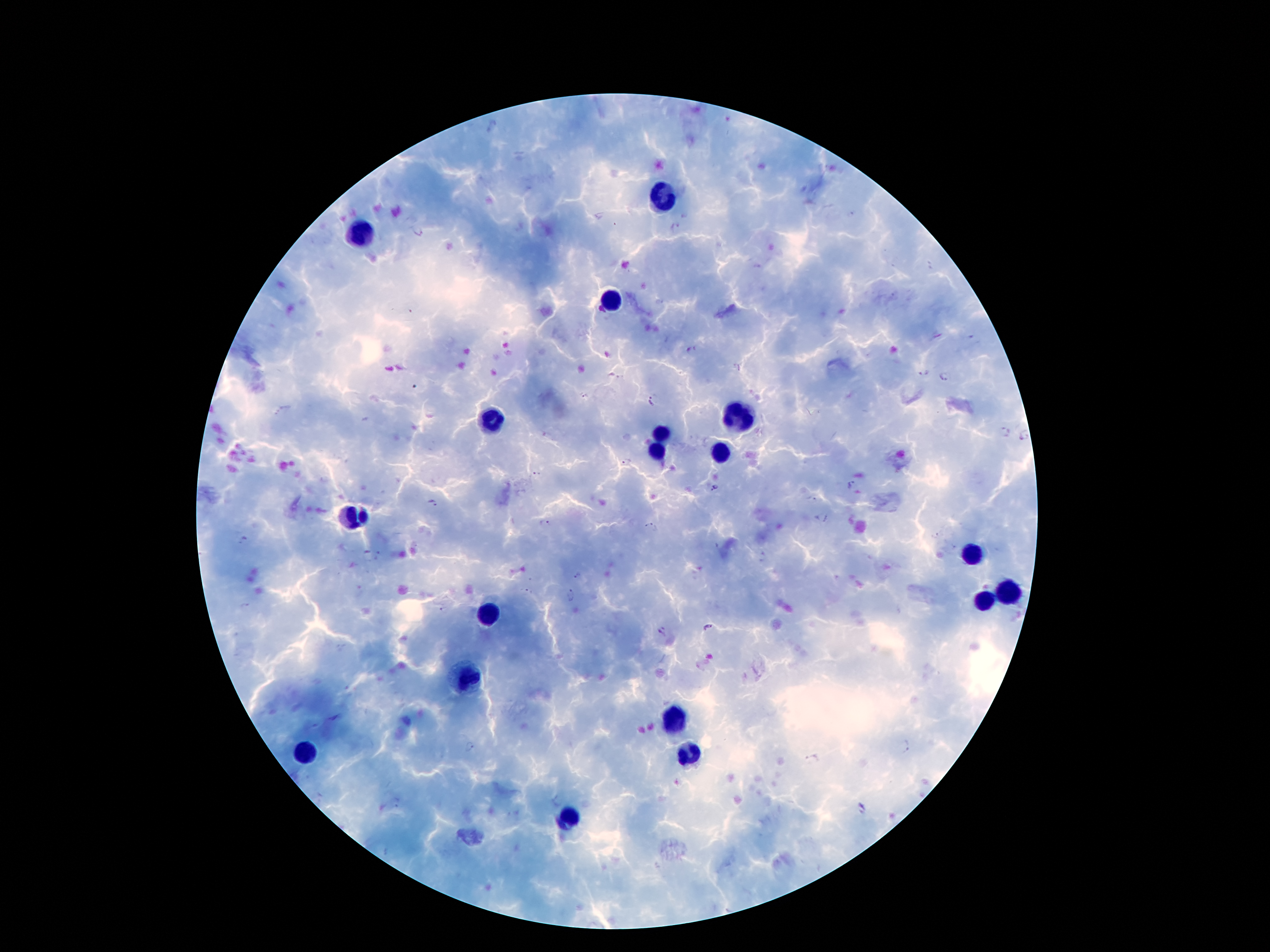
Approximate centers as {x, y} in pixels.
Summary:
  - Leukocyte locations: {665, 200}, {363, 234}, {611, 298}, {491, 419}, {739, 419}, {659, 435}, {659, 452}, {720, 456}, {351, 515}, {970, 555}, {1008, 593}, {985, 604}, {487, 616}, {464, 678}, {674, 720}, {304, 755}, {689, 755}, {567, 819}
  - Plasmodium parasite locations: {492, 128}, {675, 227}, {691, 350}, {925, 373}, {614, 377}, {943, 377}, {585, 397}, {653, 400}, {1005, 433}, {1025, 436}, {626, 462}, {537, 474}, {852, 485}, {715, 488}, {812, 499}, {432, 502}, {821, 517}, {551, 524}, {653, 527}, {243, 539}, {579, 575}, {527, 591}, {570, 595}, {442, 611}, {708, 628}, {662, 631}, {472, 747}, {904, 747}, {812, 760}, {862, 808}
  - Capture: smartphone through the microscope eyepiece
  - Field of view: single
  - Magnification: 100x
  - Image size: 1270×952 pixels
  - Stain: Giemsa
  - Patient malaria status: positive for Plasmodium falciparum
  - Preparation: thick blood film